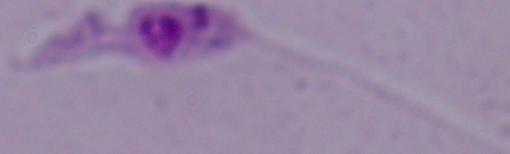
{
  "magnification": "1000x",
  "modality": "micrograph",
  "identification": "Leishmania"
}